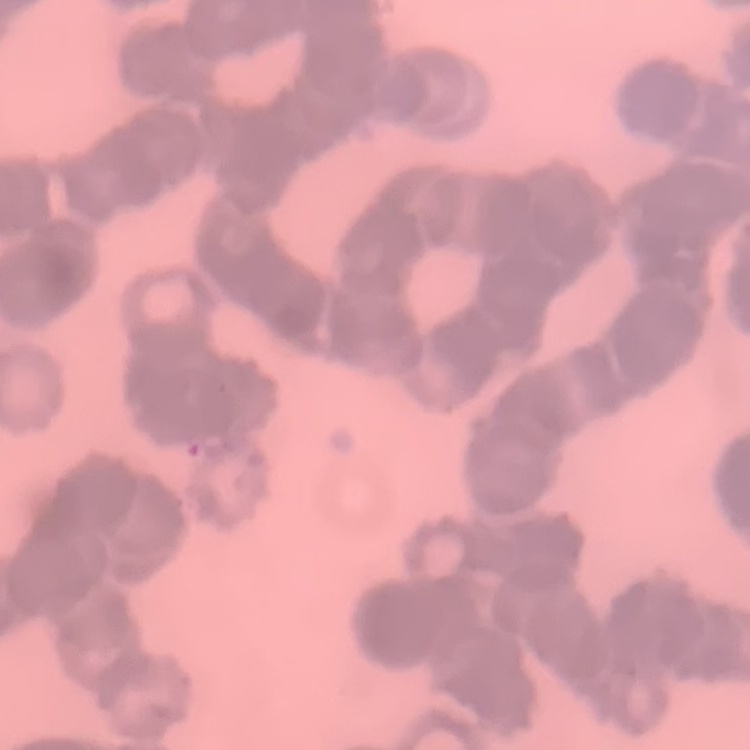

erythrocyte morphology = rouleaux formation
preparation = thin peripheral smear
image type = square crop of a larger photomicrograph
stain = Field's or Giemsa